Describe the morphology of the erythrocytes.
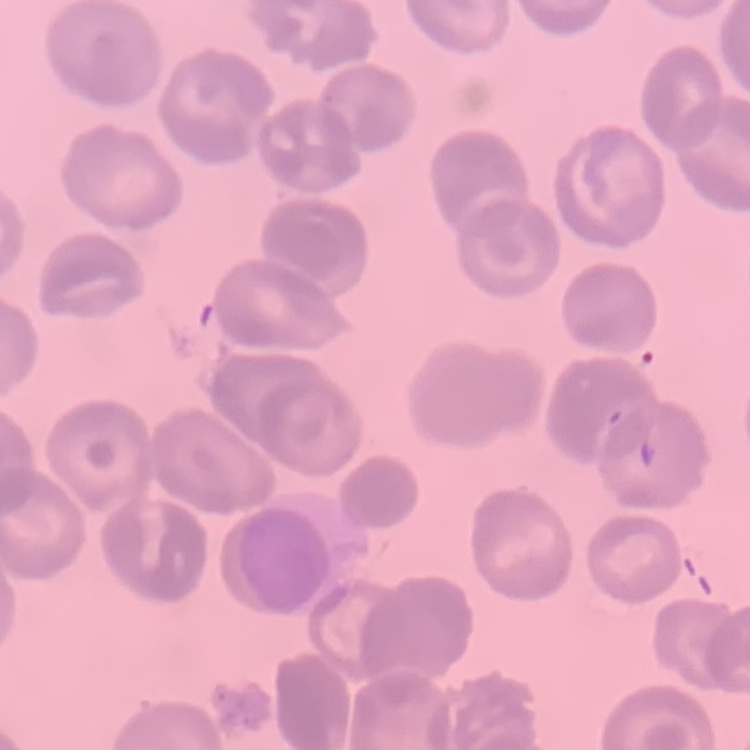

They show no rouleaux formation.

image type = one tile cut from a larger photomicrograph
stain = Field's or Giemsa
preparation = thin blood film